Locate every blood parasite and identify its species.
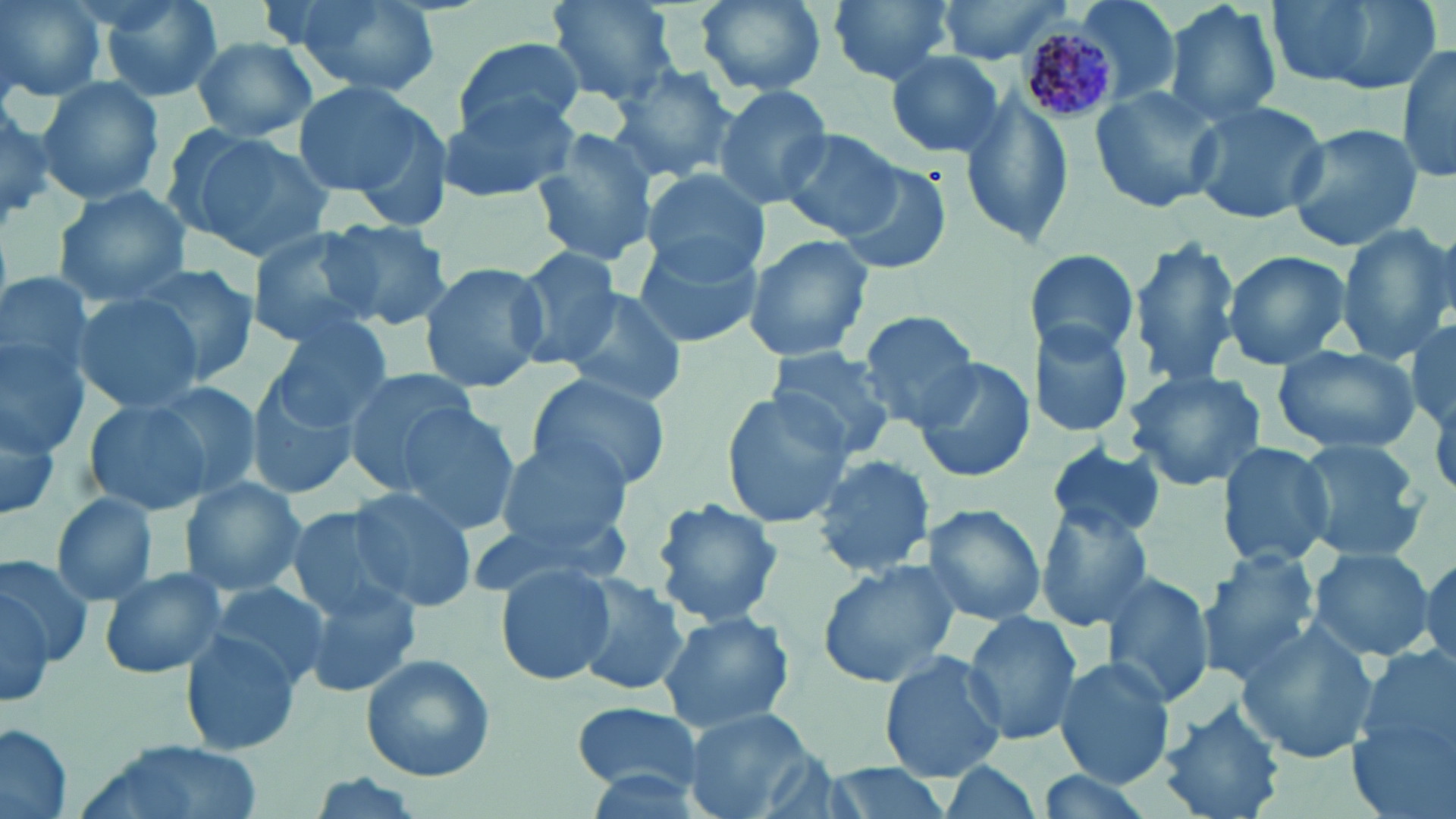

Approximate bounding boxes as (x1,y1)-(x2,y2) corner pairs in pixels.
Plasmodium malariae-infected red blood cells: (1018,26)-(1121,123).
No Plasmodium falciparum, Plasmodium ovale, Plasmodium vivax, Babesia divergens, or Trypanosoma brucei observed.

slide-level diagnosis = Plasmodium malariae
image size = 1456×819 pixels
stain = May-Grünwald-Giemsa
magnification = 1000x
preparation = thin blood film
uninfected red blood cell locations = approximate bounding boxes as (x1,y1)-(x2,y2) corner pairs in pixels: (1,0)-(106,102), (96,0)-(224,103), (549,0)-(680,106), (693,0)-(828,94), (824,0)-(959,86), (934,0)-(1074,62), (1071,0)-(1183,108), (1164,0)-(1283,130), (1263,0)-(1445,98), (284,1)-(440,95), (190,37)-(318,142), (449,39)-(585,140), (1396,44)-(1456,184), (884,49)-(1008,160), (610,66)-(740,183), (34,76)-(166,208), (290,81)-(433,199), (714,85)-(834,210), (1089,86)-(1222,213), (439,94)-(579,202), (954,95)-(1077,247), (1187,98)-(1329,225), (0,102)-(58,231), (1281,123)-(1426,252), (171,125)-(337,263), (778,128)-(905,241), (530,129)-(659,268), (836,164)-(950,275), (640,167)-(770,278), (53,185)-(192,309), (325,218)-(452,330), (1336,222)-(1453,363), (245,226)-(381,347), (628,233)-(765,351), (742,234)-(875,364), (1130,239)-(1241,390), (507,246)-(624,367), (1027,250)-(1140,362), (1221,251)-(1355,370), (131,260)-(260,392), (419,261)-(551,393), (0,268)-(95,394), (561,287)-(689,408), (73,293)-(204,414), (858,309)-(982,428), (267,318)-(395,435), (1029,323)-(1134,439), (1410,324)-(1455,434), (1,335)-(91,454), (1271,343)-(1423,458), (765,346)-(899,460), (909,355)-(1036,485), (340,366)-(482,494), (1121,367)-(1268,493), (528,372)-(670,491), (245,375)-(365,501), (147,380)-(263,498), (719,392)-(852,529), (82,395)-(222,516), (0,403)-(64,522), (389,403)-(521,538), (493,437)-(631,554), (1297,439)-(1428,562), (1215,440)-(1336,570), (1044,442)-(1167,540), (811,454)-(938,576), (178,476)-(306,596), (345,487)-(480,611), (51,491)-(156,605), (652,497)-(784,627), (917,504)-(1048,626), (284,506)-(413,624), (1034,507)-(1157,630), (1307,545)-(1435,664), (1197,548)-(1322,681), (1418,548)-(1455,677), (0,554)-(94,666), (815,559)-(961,688), (496,560)-(618,688), (98,565)-(228,679), (1098,572)-(1215,710), (573,575)-(691,696), (302,577)-(421,699), (207,581)-(330,687), (0,587)-(55,703), (655,610)-(797,734), (962,611)-(1086,745), (1237,623)-(1381,764), (181,634)-(303,754), (1352,648)-(1455,789), (880,652)-(1006,780), (360,653)-(496,782), (1054,657)-(1176,788), (1158,699)-(1287,819), (568,701)-(705,794), (682,708)-(820,819), (0,723)-(74,817), (74,740)-(265,819), (935,761)-(1048,819), (814,764)-(956,817), (1032,771)-(1163,819)
field of view = one of a larger specimen
modality = optical microscopy